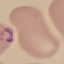

Summary:
  - Result: malaria parasites identified
  - Preparation: thin blood smear
  - Stain: Giemsa
  - Capture: smartphone through the microscope eyepiece
  - Image type: automatically extracted cell patch, resized to 64 × 64 pixels